Evaluate for parasitized red blood cells.
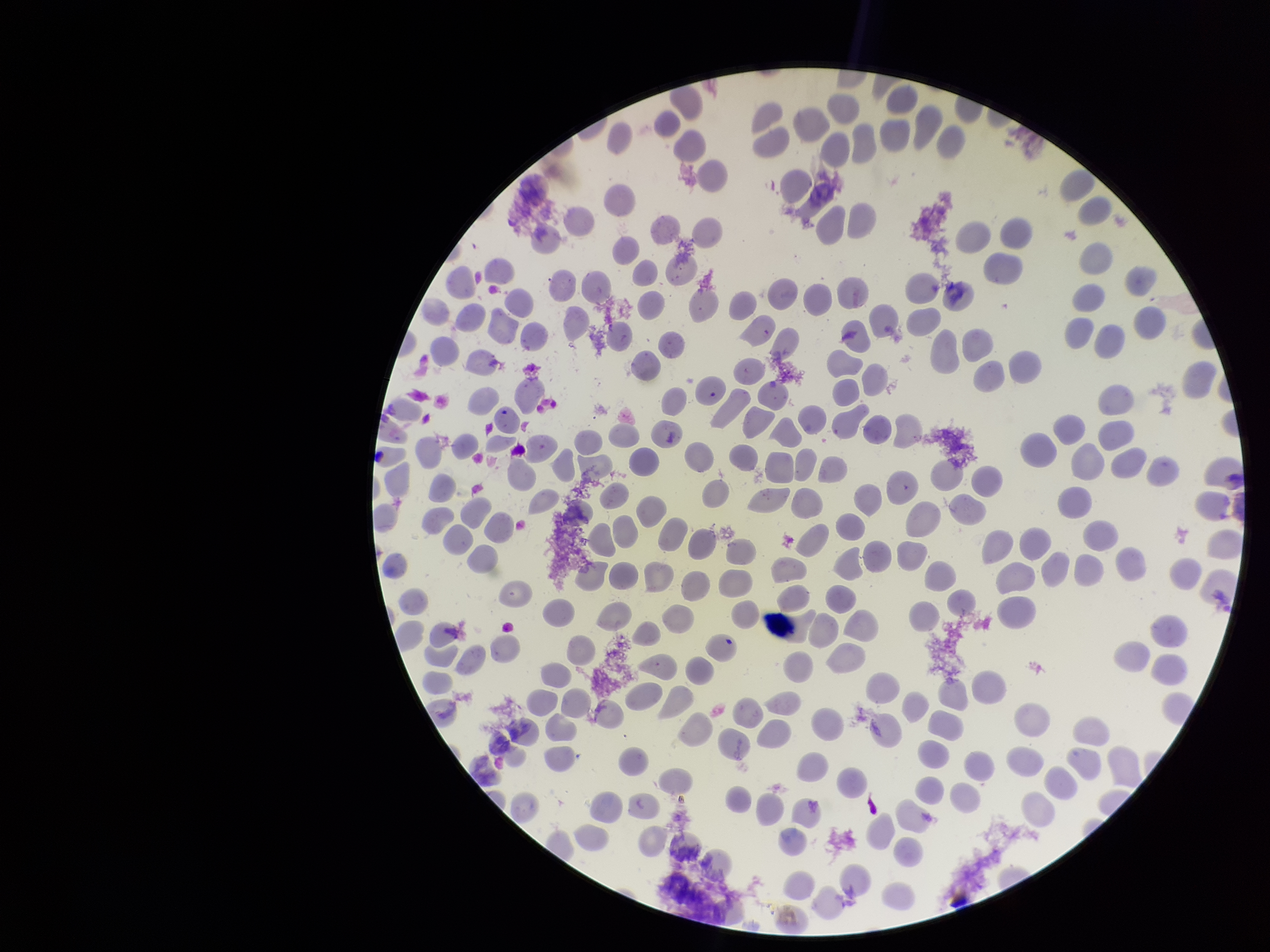
None seen.

Preparation: thin. Parasitized red blood cell count: 0. Image is 1270×952 pixels. One field from this slide. Species reported for this patient: Plasmodium vivax. Photographed through the microscope eyepiece with a smartphone camera. Patient malaria status: infected. Red blood cell count: 246. Giemsa stain.